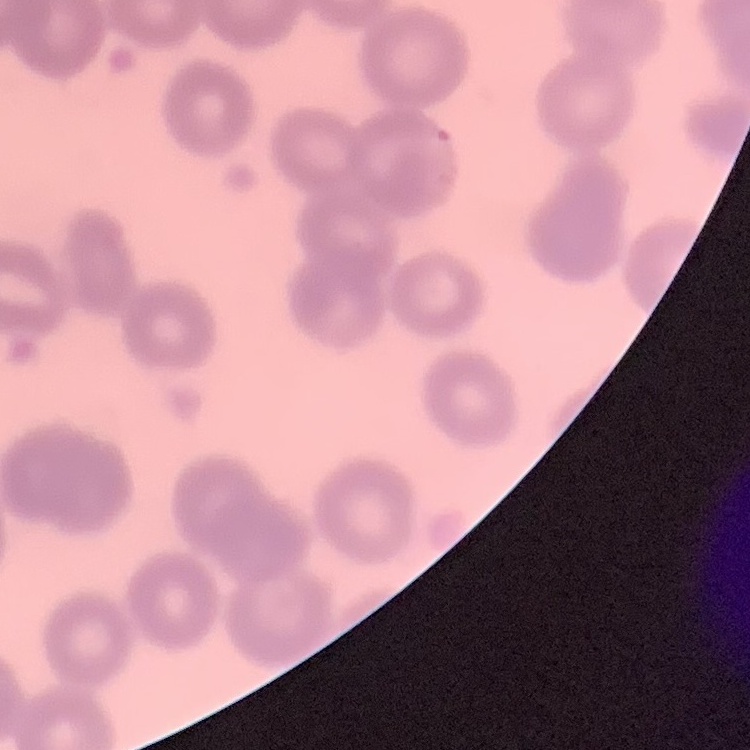
Summary:
  - Red blood cell morphology: no rouleaux formation
  - Image type: square crop of a larger photomicrograph
  - Stain: Field's or Giemsa
  - Preparation: thin blood film